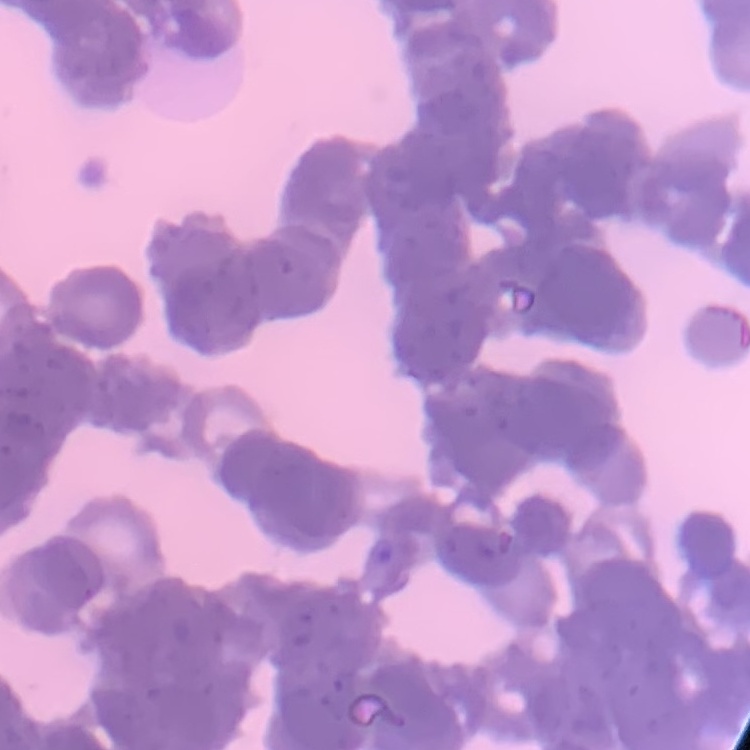

erythrocyte_morphology: rouleaux formation
image_type: one tile cut from a larger photomicrograph
stain: Field's or Giemsa
preparation: thin blood film